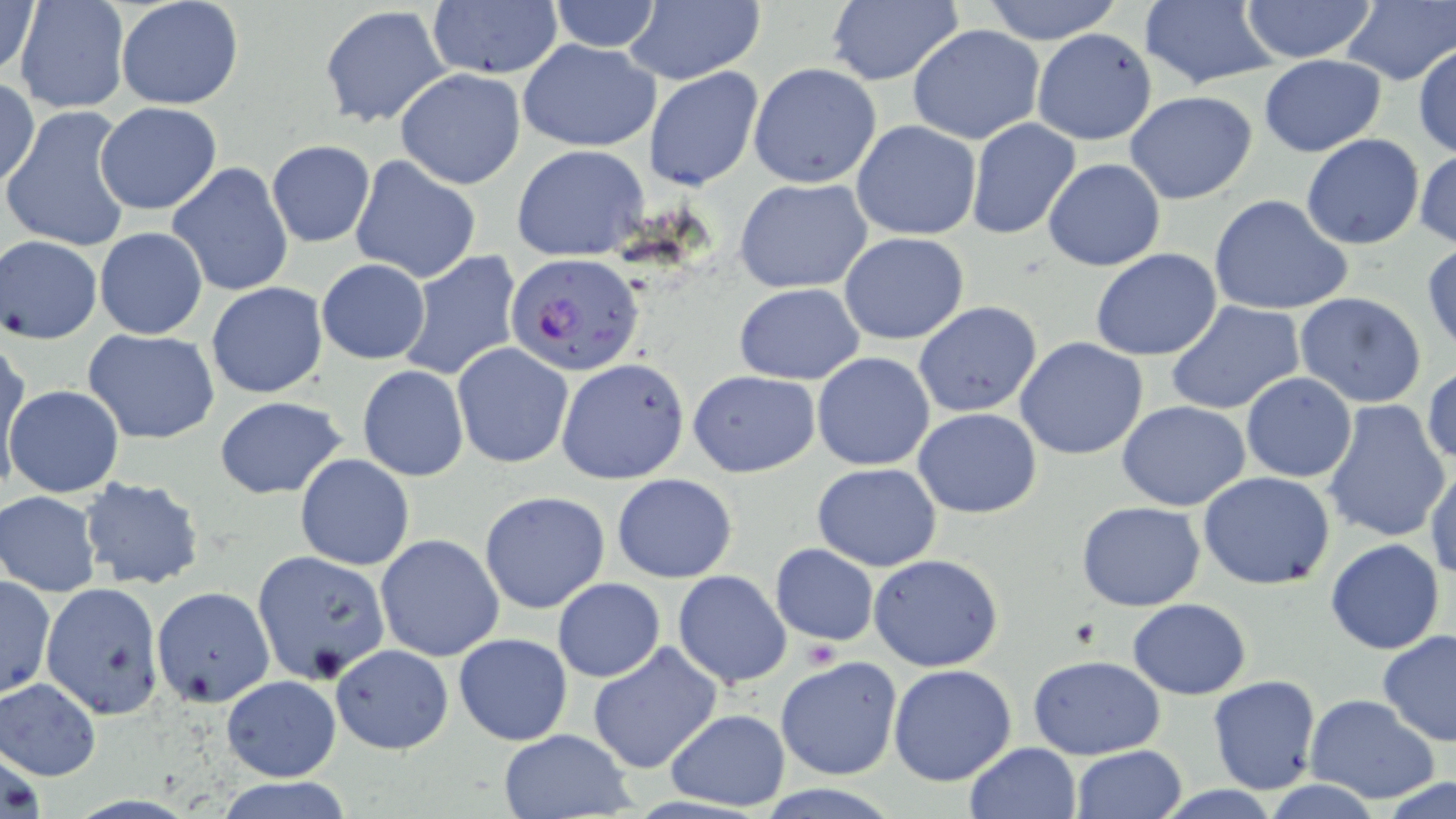

Summary:
  - Coordinate format: approximate bounding boxes as (x1,y1)-(x2,y2) corner pairs in pixels
  - Platelet locations: (804,638)-(842,668)
  - Uninfected red blood cell locations: (0,0)-(43,86), (12,0)-(131,115), (116,0)-(244,110), (545,0)-(662,53), (624,0)-(765,85), (978,0)-(1124,45), (1137,0)-(1279,91), (1240,0)-(1379,62), (1338,0)-(1455,86), (824,1)-(965,87), (425,2)-(564,81), (319,6)-(449,127), (907,23)-(1045,144), (1032,28)-(1157,146), (518,39)-(662,153), (1413,43)-(1456,159), (1259,54)-(1387,156), (749,62)-(882,188), (644,66)-(763,192), (394,68)-(528,189), (1,78)-(40,193), (1124,92)-(1258,205), (95,101)-(221,214), (3,105)-(135,253), (965,117)-(1081,240), (851,120)-(983,240), (1301,133)-(1426,249), (266,141)-(376,248), (513,145)-(651,262), (1414,149)-(1456,253), (348,155)-(480,283), (1042,158)-(1165,271), (167,162)-(293,297), (735,178)-(874,293), (1208,195)-(1355,316), (94,227)-(208,340), (839,232)-(969,344), (2,235)-(102,343), (1424,243)-(1456,350), (1090,249)-(1222,362), (397,250)-(524,383), (316,258)-(432,364), (1049,259)-(1193,403), (204,281)-(328,399), (734,283)-(863,384), (1294,293)-(1428,408), (1164,301)-(1306,416), (914,302)-(1043,418), (84,330)-(222,444), (1,335)-(29,479), (1015,336)-(1149,460), (451,341)-(574,469), (812,353)-(936,471), (556,358)-(690,484), (1423,364)-(1456,469), (357,367)-(469,481), (688,371)-(821,476), (1241,373)-(1357,482), (5,384)-(124,499), (214,395)-(349,499), (1321,399)-(1451,543), (1118,401)-(1251,511), (913,409)-(1042,518), (294,452)-(415,571), (1425,459)-(1456,584), (812,462)-(941,572), (1198,472)-(1336,590), (612,473)-(739,583), (78,476)-(206,591), (479,490)-(611,614), (3,491)-(100,596), (1077,501)-(1206,611), (375,534)-(506,662), (1325,538)-(1445,655), (770,543)-(878,645), (250,549)-(391,684), (867,554)-(1005,672), (673,569)-(791,689), (1,576)-(54,699), (552,577)-(665,682), (40,582)-(164,719), (151,587)-(273,708), (1129,598)-(1251,698), (1376,630)-(1456,746), (452,632)-(573,746), (330,643)-(453,754), (587,643)-(723,775), (1029,653)-(1165,761), (776,656)-(903,781), (888,664)-(1017,785), (222,674)-(340,782), (1207,674)-(1322,794), (1,677)-(101,781), (1304,695)-(1441,804), (664,707)-(791,811), (497,729)-(636,818), (963,742)-(1082,819), (1070,746)-(1188,819), (210,775)-(354,818), (1379,779)-(1456,819)
  - Plasmodium falciparum-infected red blood cell locations: (507,253)-(643,377)
  - Slide-level diagnosis: Plasmodium falciparum
  - Field of view: one of a larger specimen
  - Stain: May-Grünwald-Giemsa
  - Image size: 1456×819 pixels
  - Magnification: 1000x
  - Preparation: thin blood film
  - Modality: optical microscopy